Name the parasite shown.
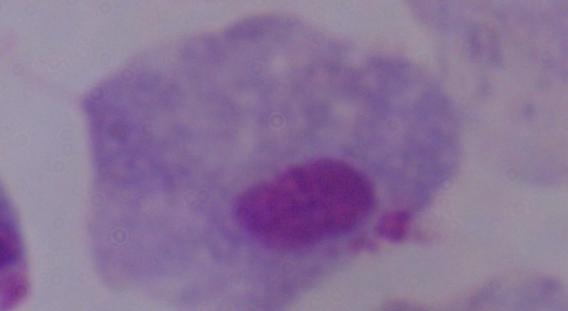

This is a trichomonad.

Captured at 1000x magnification. Micrograph.